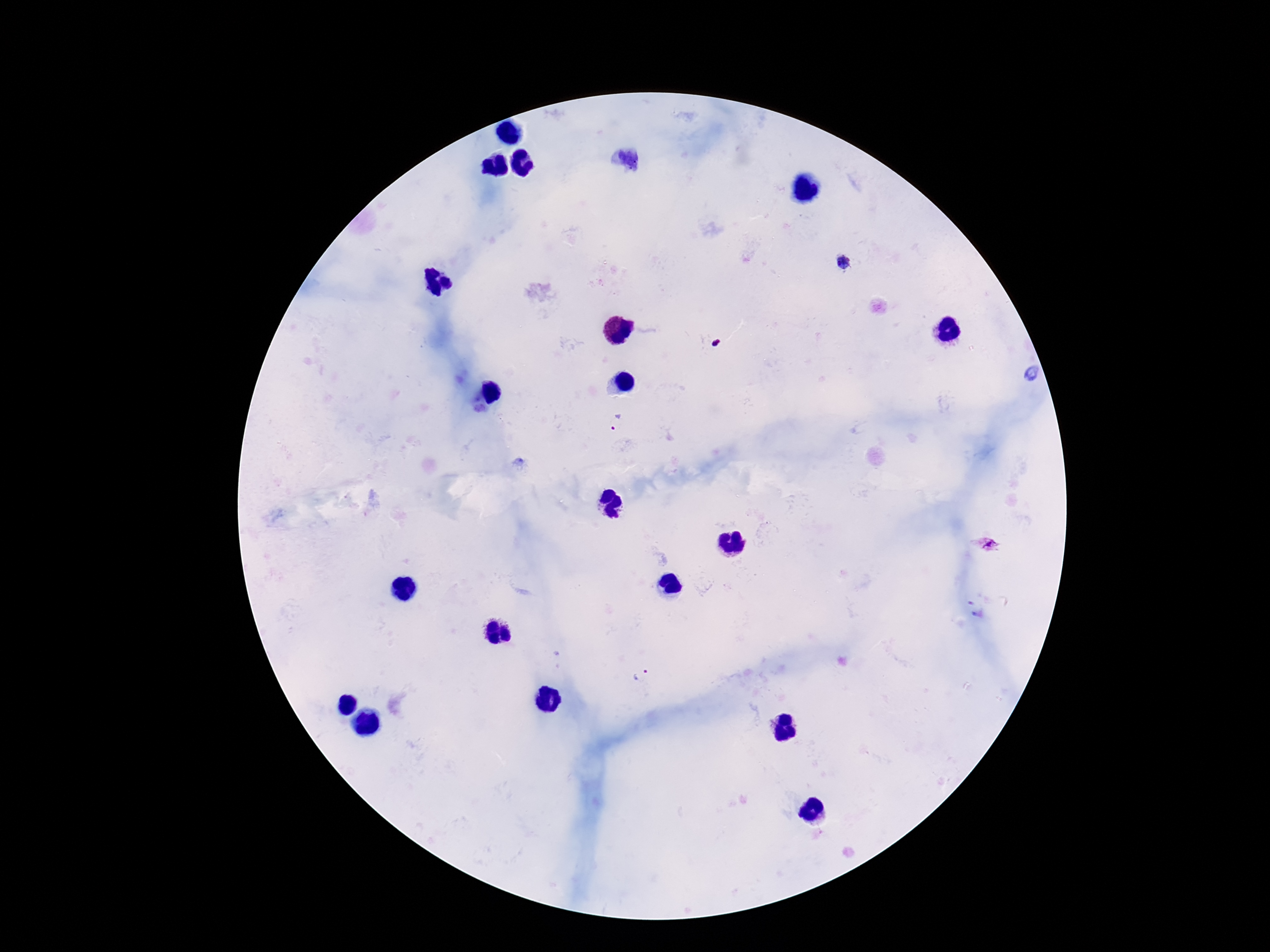
Approximate centers as [x, y] in pixels. Plasmodium parasite locations: [626, 159], [842, 263], [715, 344], [616, 422], [987, 545], [641, 676]. Patient malaria status: positive. Giemsa stain. Thick blood film. Image is 1270×952 pixels. One field from this slide. Photographed through the microscope eyepiece with a smartphone camera. 100x magnification.